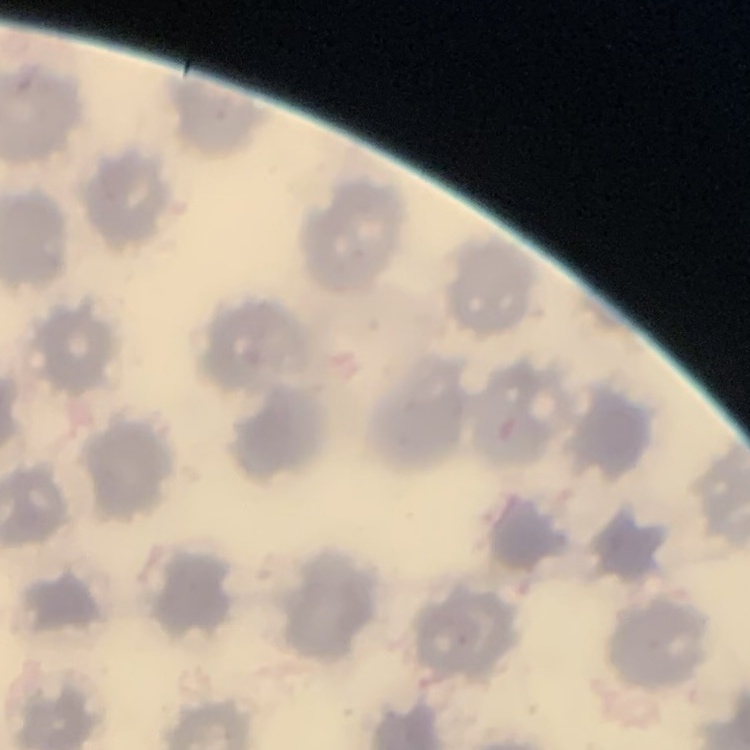
red blood cell morphology = no rouleaux formation
stain = Field's or Giemsa
preparation = thin blood film
image type = one tile cut from a larger photomicrograph